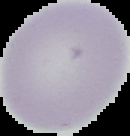

Summary:
  - Image type: segmented cell region on a black background
  - Result: no Plasmodium parasites detected
  - Preparation: thin blood film
  - Image size: 130×136 pixels